Identify the parasite.
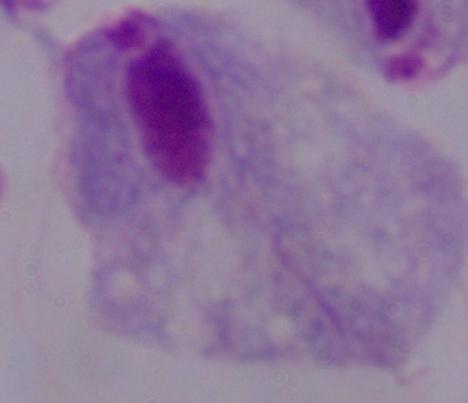
A trichomonad.

1000x magnification. Photomicrograph.